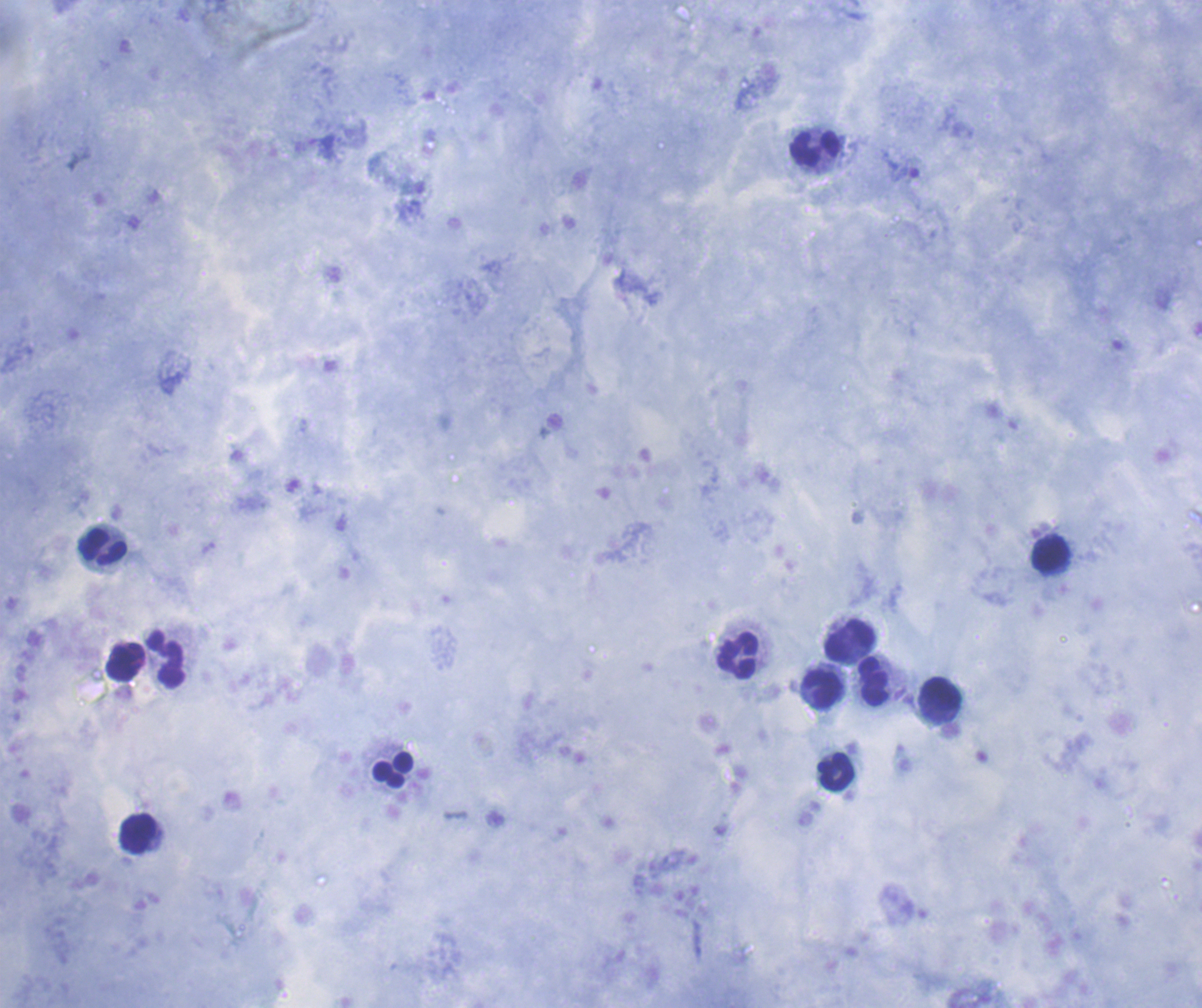

preparation: thick smear of blood
coloration_quality: good
result: no malaria parasites detected
background_quality: good
leukocyte_locations: 'approximate centers as {x, y} in pixels: {816, 149}, {102, 547}, {1050, 553}, {851, 641}, {737, 655}, {167, 659}, {126, 662}, {874, 681}, {821, 690}, {941, 693}, {392, 770}, {836, 772}, {138, 833}'
stain: Romanowsky
magnification: 100x
field_of_view: one from this slide
image_size: 1202×1008 pixels
context: previously used in an actual diagnosis